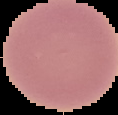

{
  "result": "no Plasmodium parasites seen",
  "preparation": "thin blood smear",
  "image_type": "segmented cell region with the area outside set to black",
  "image_size": "118×115 pixels"
}